Classify this cell by malaria status.
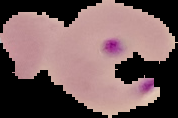
It is parasitized.

image type = cell region segmented out of the field of view; surrounding area masked to black
preparation = thin blood smear
image size = 178×118 pixels